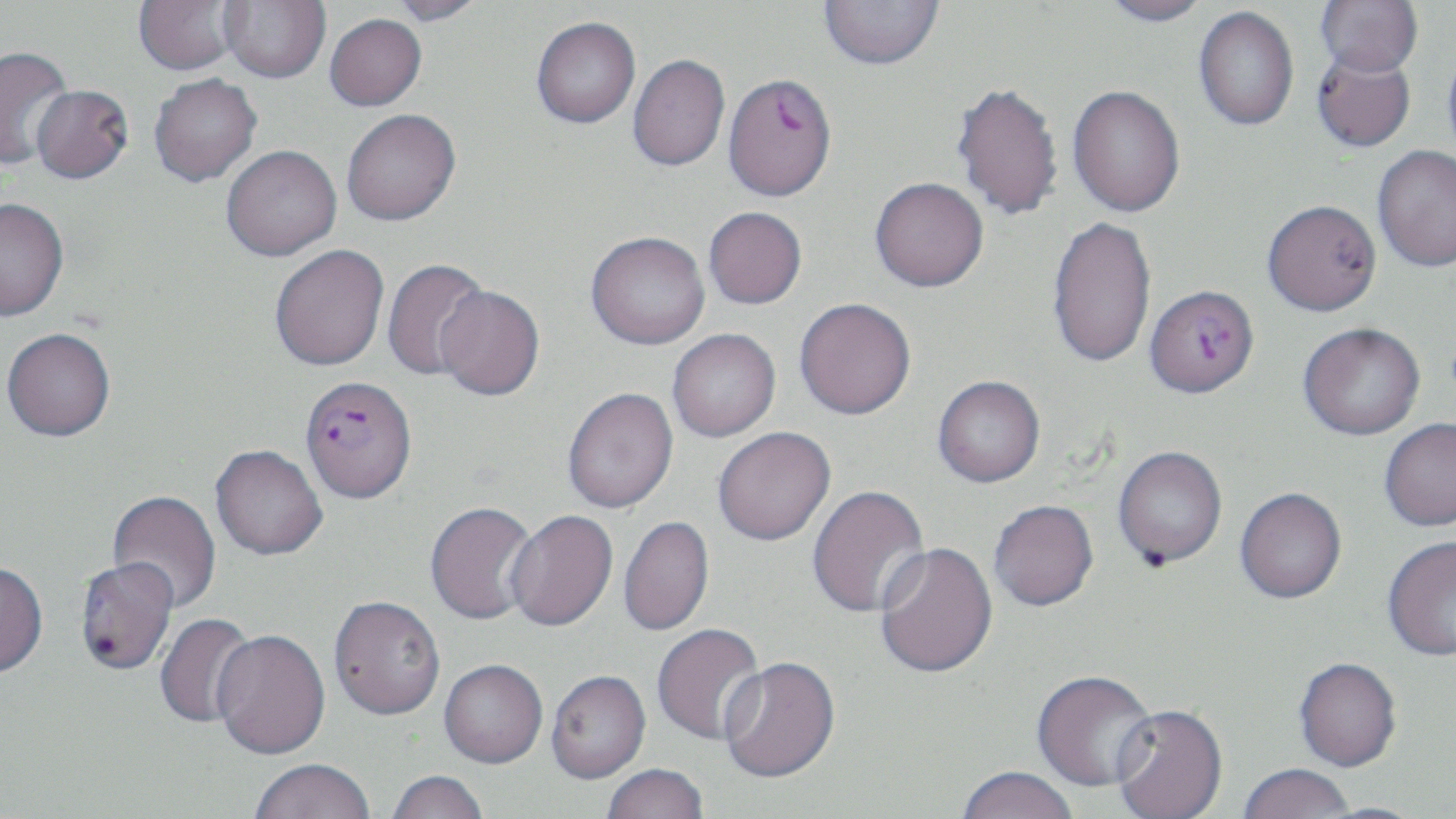

{
  "slide_level_diagnosis": "Plasmodium falciparum",
  "uninfected_red_blood_cell_locations": "approximate bounding boxes as [x1, y1, x2, y2] in pixels: [133, 0, 243, 75], [219, 0, 330, 83], [387, 0, 490, 26], [818, 0, 945, 70], [1097, 0, 1214, 27], [1315, 0, 1423, 77], [1194, 6, 1299, 131], [324, 13, 427, 111], [530, 16, 640, 128], [1442, 37, 1456, 167], [0, 45, 73, 171], [1311, 48, 1417, 152], [627, 54, 730, 171], [148, 73, 262, 187], [951, 81, 1064, 221], [30, 84, 134, 183], [1068, 85, 1186, 217], [341, 109, 461, 226], [221, 145, 341, 261], [1372, 145, 1456, 272], [870, 177, 989, 292], [0, 198, 69, 321], [1262, 199, 1381, 315], [703, 206, 807, 309], [1047, 215, 1157, 369], [586, 231, 709, 349], [269, 245, 389, 371], [381, 258, 491, 381], [434, 285, 545, 401], [794, 298, 916, 420], [1298, 322, 1425, 440], [2, 328, 116, 443], [667, 329, 781, 442], [932, 375, 1045, 488], [562, 388, 678, 515], [1379, 418, 1456, 531], [712, 427, 837, 547], [210, 446, 328, 562], [1113, 446, 1228, 570], [807, 485, 931, 620], [1235, 489, 1347, 606], [107, 491, 221, 613], [989, 502, 1099, 614], [425, 503, 539, 627], [504, 511, 618, 635], [618, 517, 715, 637], [1382, 535, 1456, 662], [875, 542, 999, 681], [0, 563, 48, 682], [329, 599, 446, 724], [154, 612, 259, 729], [652, 624, 767, 746], [211, 632, 331, 761], [719, 659, 841, 787], [1293, 659, 1402, 774], [439, 662, 547, 771], [546, 673, 651, 786], [1030, 673, 1159, 794], [1111, 707, 1229, 819], [250, 761, 375, 818], [603, 766, 709, 819], [1238, 766, 1354, 819], [956, 769, 1078, 819], [386, 772, 488, 819]",
  "magnification": "1000x",
  "stain": "May-Grünwald-Giemsa",
  "modality": "optical microscopy",
  "field_of_view": "one of a larger specimen",
  "preparation": "thin blood smear",
  "plasmodium_falciparum_infected_red_blood_cell_locations": "approximate bounding boxes as [x1, y1, x2, y2] in pixels: [722, 72, 837, 201], [1145, 284, 1260, 398], [300, 375, 417, 505], [74, 560, 179, 678]",
  "image_size": "1456×819 pixels"
}